Report the malaria status of this cell.
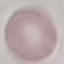

Uninfected.

capture: smartphone camera at the microscope eyepiece
preparation: thin smear
image_type: cell patch, automatically extracted from a larger field of view and resized to 64 × 64 pixels
stain: Giemsa